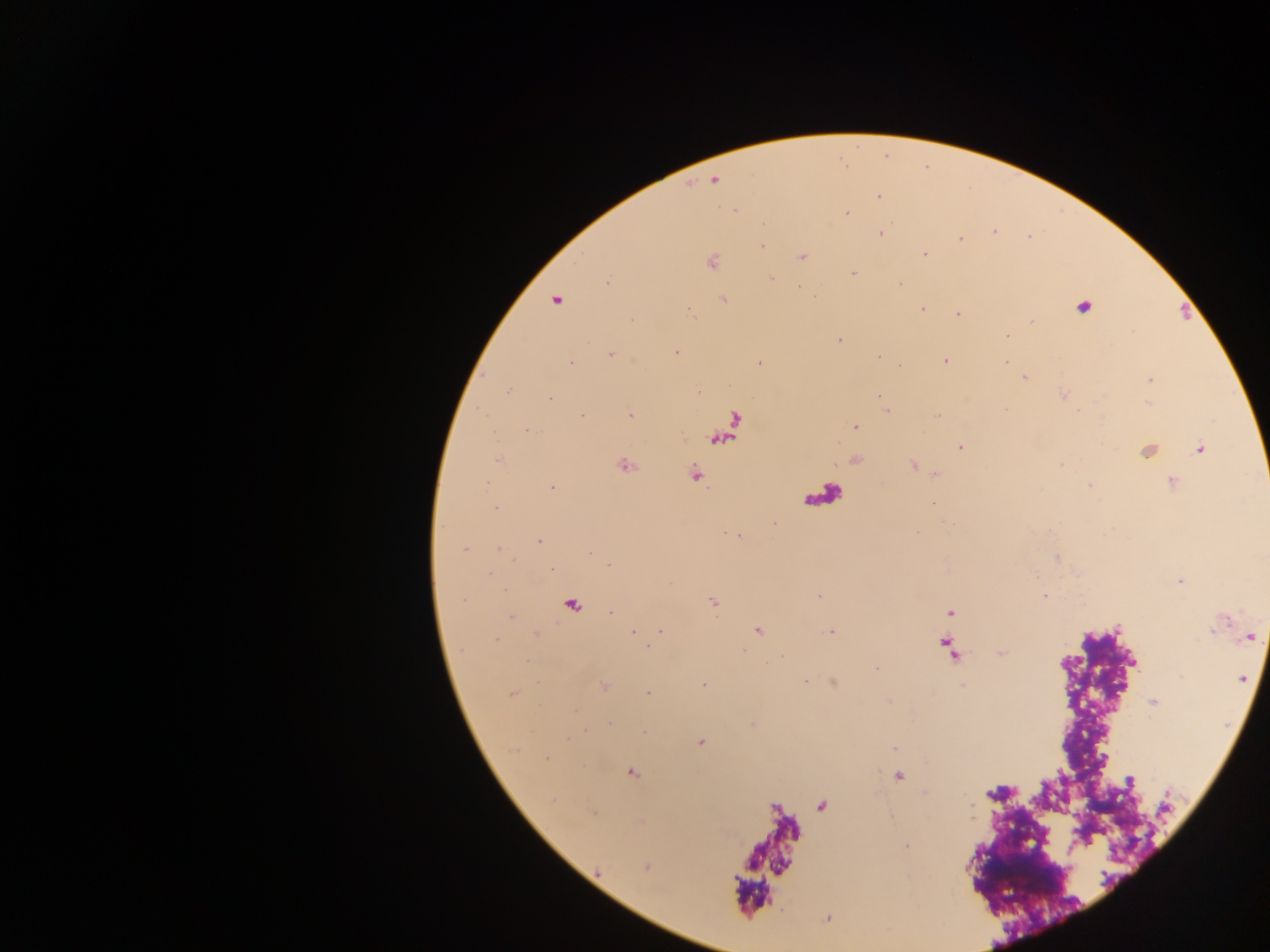

Approximate centers as x y in pixels.
Summary:
  - Plasmodium parasite locations: 714 181; 879 196; 735 210; 846 212; 994 231; 880 233; 960 239; 762 246; 924 253; 802 256; 711 261; 853 273; 771 279; 607 281; 899 283; 813 296; 556 299; 722 299; 1083 306; 921 308; 688 309; 957 313; 1007 336; 839 341; 676 352; 610 353; 878 356; 944 360; 1005 361; 571 362; 759 362; 900 366; 1025 376; 1150 379; 508 390; 698 391; 878 395; 1063 395; 550 397; 886 410; 582 415; 630 415; 937 416; 855 426; 526 429; 960 447; 1200 448; 1147 449; 498 459; 855 459; 624 464; 914 465; 935 472; 694 474; 1172 481; 1089 486; 551 487; 932 502; 496 507; 729 533; 538 541; 463 549; 551 568; 1180 580; 819 596; 1044 596; 712 602; 570 604; 949 612; 511 616; 757 629; 830 630; 631 631; 660 631; 1250 636; 647 646; 877 668; 1240 679; 805 680; 604 685; 704 685; 512 693; 647 693; 1154 702; 700 741; 630 772; 899 775; 646 867; 826 917
  - Leukocyte locations: 822 495; 768 860
  - Field of view: single
  - Image size: 1270×952 pixels
  - Preparation: thick blood smear
  - Country: Ghana
  - Capture: mobile-phone photograph through a microscope